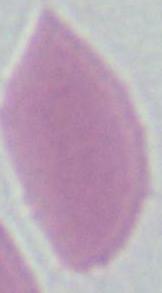
Summary:
  - Magnification: 1000x
  - Modality: photomicrograph
  - Identification: red blood cell